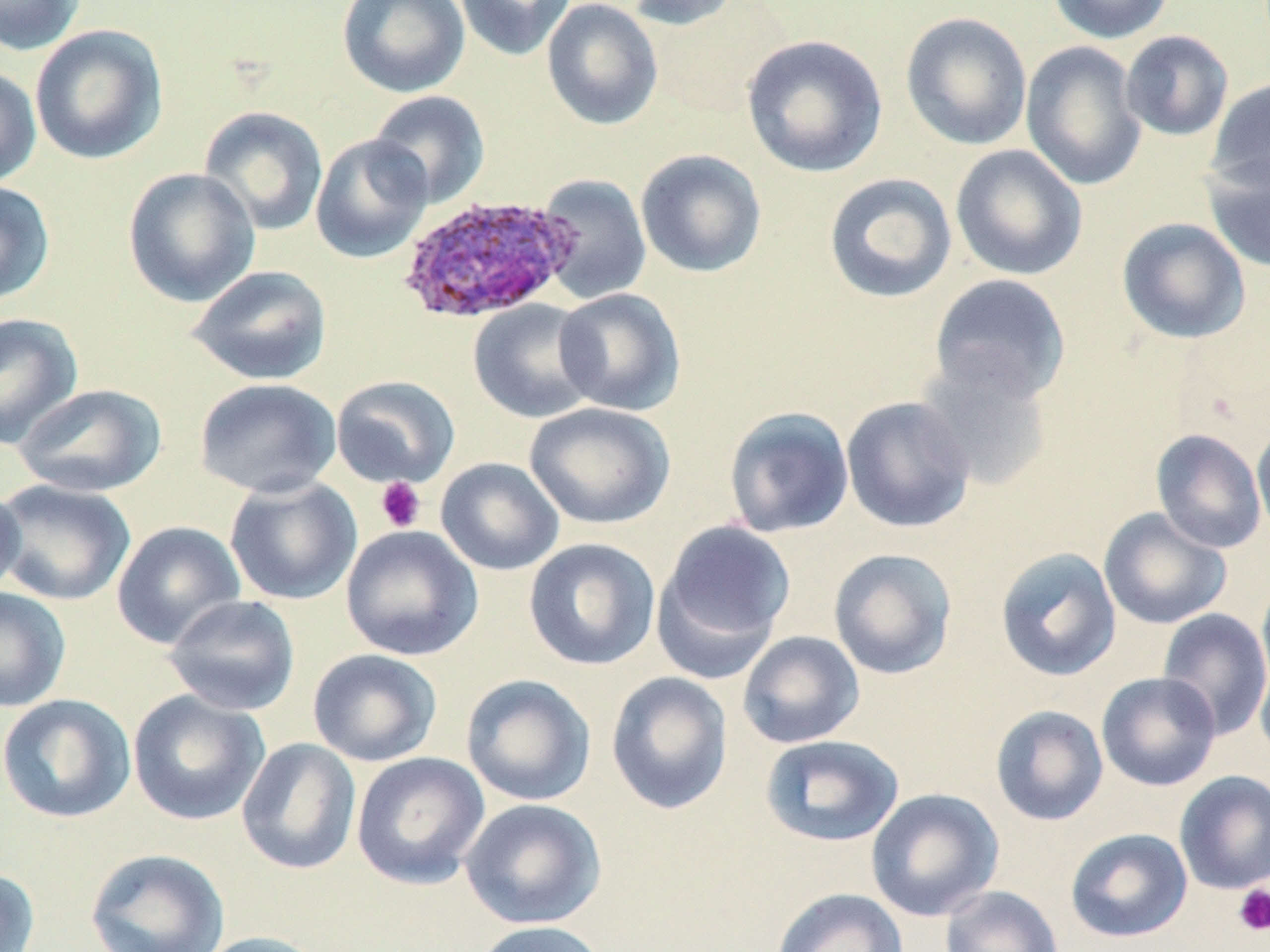
Approximate bounding boxes as named x1/y1/x2/y2 corners in pixels. Platelet locations: (x1=374, y1=477, x2=426, y2=533), (x1=1232, y1=884, x2=1270, y2=936). Uninfected red blood cell locations: (x1=0, y1=0, x2=85, y2=56), (x1=336, y1=0, x2=470, y2=98), (x1=454, y1=0, x2=576, y2=61), (x1=541, y1=0, x2=663, y2=130), (x1=624, y1=0, x2=745, y2=30), (x1=1047, y1=0, x2=1174, y2=44), (x1=900, y1=12, x2=1033, y2=151), (x1=29, y1=24, x2=169, y2=165), (x1=1120, y1=30, x2=1234, y2=141), (x1=741, y1=34, x2=888, y2=178), (x1=1020, y1=41, x2=1148, y2=191), (x1=0, y1=67, x2=42, y2=188), (x1=1207, y1=77, x2=1270, y2=192), (x1=367, y1=90, x2=490, y2=209), (x1=198, y1=106, x2=329, y2=236), (x1=310, y1=134, x2=433, y2=264), (x1=950, y1=144, x2=1088, y2=281), (x1=635, y1=149, x2=767, y2=278), (x1=1202, y1=154, x2=1270, y2=273), (x1=122, y1=167, x2=260, y2=307), (x1=823, y1=172, x2=958, y2=304), (x1=535, y1=174, x2=652, y2=303), (x1=0, y1=180, x2=55, y2=307), (x1=1116, y1=217, x2=1251, y2=345), (x1=186, y1=264, x2=333, y2=386), (x1=928, y1=273, x2=1071, y2=406), (x1=554, y1=288, x2=686, y2=416), (x1=467, y1=299, x2=601, y2=424), (x1=0, y1=312, x2=83, y2=450), (x1=914, y1=354, x2=1054, y2=492), (x1=331, y1=375, x2=461, y2=489), (x1=194, y1=377, x2=342, y2=499), (x1=13, y1=383, x2=166, y2=498), (x1=841, y1=396, x2=976, y2=534), (x1=524, y1=402, x2=675, y2=529), (x1=722, y1=405, x2=855, y2=538), (x1=1252, y1=419, x2=1270, y2=543), (x1=1151, y1=429, x2=1267, y2=553), (x1=435, y1=457, x2=564, y2=576), (x1=224, y1=476, x2=362, y2=605), (x1=0, y1=479, x2=137, y2=606), (x1=0, y1=481, x2=26, y2=603), (x1=1098, y1=507, x2=1232, y2=630), (x1=654, y1=519, x2=796, y2=673), (x1=112, y1=521, x2=245, y2=649), (x1=340, y1=524, x2=484, y2=661), (x1=523, y1=537, x2=660, y2=671), (x1=995, y1=547, x2=1122, y2=682), (x1=827, y1=548, x2=958, y2=680), (x1=1256, y1=574, x2=1270, y2=702), (x1=0, y1=587, x2=71, y2=712), (x1=163, y1=594, x2=301, y2=716), (x1=1157, y1=607, x2=1270, y2=741), (x1=736, y1=630, x2=865, y2=749), (x1=307, y1=648, x2=443, y2=767), (x1=1255, y1=657, x2=1270, y2=765), (x1=606, y1=670, x2=734, y2=815), (x1=1096, y1=672, x2=1221, y2=791), (x1=460, y1=673, x2=596, y2=807), (x1=127, y1=689, x2=270, y2=826), (x1=0, y1=693, x2=136, y2=823), (x1=990, y1=704, x2=1109, y2=826), (x1=760, y1=734, x2=904, y2=847), (x1=236, y1=737, x2=362, y2=875), (x1=351, y1=751, x2=490, y2=890), (x1=1174, y1=770, x2=1270, y2=894), (x1=865, y1=787, x2=1004, y2=922), (x1=459, y1=798, x2=607, y2=930), (x1=1065, y1=828, x2=1193, y2=943), (x1=85, y1=847, x2=229, y2=952), (x1=0, y1=868, x2=40, y2=952), (x1=940, y1=885, x2=1063, y2=952), (x1=771, y1=887, x2=909, y2=952), (x1=471, y1=920, x2=612, y2=952), (x1=192, y1=931, x2=333, y2=952). Plasmodium ovale-infected red blood cell locations: (x1=396, y1=194, x2=578, y2=325). Slide-level diagnosis: Plasmodium ovale. Single field of view. Thin blood smear. 1000x magnification. Image is 1270×952 pixels. May-Grünwald-Giemsa stain. Optical microscopy.